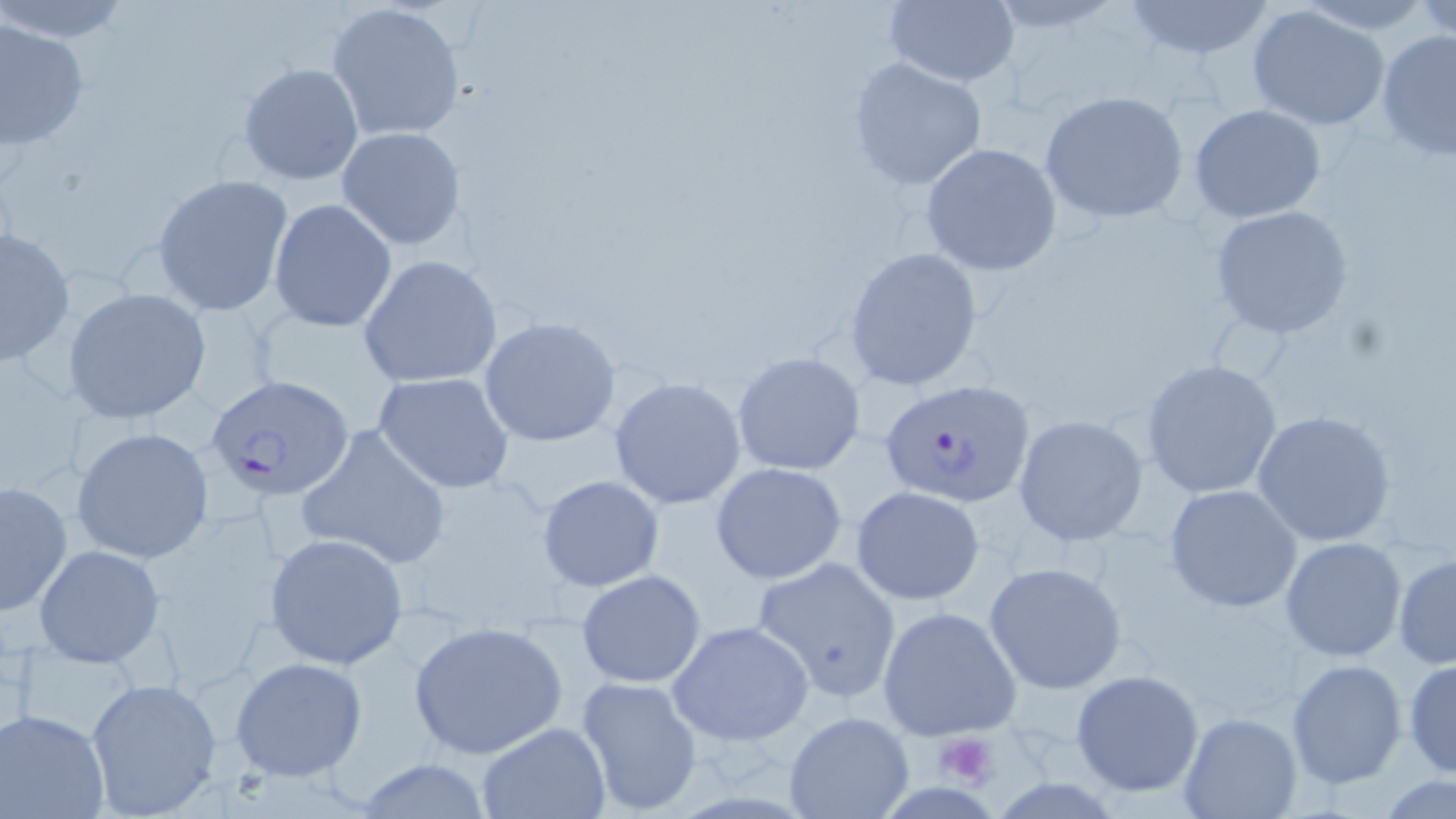

slide-level diagnosis = Plasmodium falciparum
field of view = one of a larger specimen
platelet locations = approximate bounding boxes as named x1/y1/x2/y2 corners in pixels: (x1=934, y1=731, x2=999, y2=787)
modality = light microscopy
image size = 1456×819 pixels
stain = May-Grünwald-Giemsa
uninfected red blood cell locations = approximate bounding boxes as named x1/y1/x2/y2 corners in pixels: (x1=1, y1=0, x2=133, y2=43), (x1=1416, y1=0, x2=1455, y2=40), (x1=325, y1=1, x2=469, y2=143), (x1=882, y1=1, x2=1021, y2=87), (x1=1118, y1=1, x2=1278, y2=60), (x1=1246, y1=5, x2=1392, y2=132), (x1=0, y1=17, x2=89, y2=151), (x1=1375, y1=29, x2=1456, y2=160), (x1=847, y1=58, x2=987, y2=192), (x1=238, y1=62, x2=364, y2=187), (x1=1039, y1=90, x2=1191, y2=225), (x1=1189, y1=103, x2=1328, y2=224), (x1=336, y1=125, x2=467, y2=249), (x1=920, y1=142, x2=1062, y2=277), (x1=150, y1=173, x2=295, y2=316), (x1=268, y1=198, x2=397, y2=334), (x1=1209, y1=205, x2=1356, y2=339), (x1=0, y1=226, x2=76, y2=368), (x1=844, y1=246, x2=986, y2=391), (x1=358, y1=254, x2=503, y2=389), (x1=63, y1=287, x2=212, y2=426), (x1=478, y1=316, x2=625, y2=449), (x1=733, y1=351, x2=867, y2=477), (x1=1140, y1=358, x2=1283, y2=499), (x1=372, y1=372, x2=516, y2=494), (x1=608, y1=377, x2=747, y2=509), (x1=1251, y1=409, x2=1398, y2=548), (x1=1012, y1=414, x2=1150, y2=546), (x1=297, y1=422, x2=451, y2=569), (x1=71, y1=426, x2=216, y2=565), (x1=710, y1=462, x2=849, y2=585), (x1=538, y1=474, x2=665, y2=592), (x1=0, y1=480, x2=73, y2=616), (x1=1164, y1=484, x2=1304, y2=614), (x1=850, y1=486, x2=987, y2=605), (x1=264, y1=533, x2=409, y2=670), (x1=1279, y1=536, x2=1407, y2=663), (x1=34, y1=544, x2=163, y2=667), (x1=1392, y1=553, x2=1456, y2=670), (x1=750, y1=555, x2=905, y2=705), (x1=984, y1=560, x2=1128, y2=694), (x1=576, y1=569, x2=706, y2=688), (x1=877, y1=605, x2=1023, y2=741), (x1=410, y1=619, x2=569, y2=761), (x1=667, y1=620, x2=814, y2=746), (x1=229, y1=656, x2=369, y2=783), (x1=1285, y1=658, x2=1407, y2=790), (x1=1403, y1=658, x2=1455, y2=779), (x1=1070, y1=669, x2=1205, y2=796), (x1=575, y1=675, x2=704, y2=813), (x1=84, y1=677, x2=224, y2=815), (x1=0, y1=709, x2=113, y2=819), (x1=784, y1=712, x2=913, y2=819), (x1=1177, y1=712, x2=1303, y2=818), (x1=474, y1=722, x2=612, y2=819), (x1=351, y1=759, x2=496, y2=817), (x1=1375, y1=775, x2=1456, y2=819)
preparation = thin blood film
Plasmodium falciparum-infected red blood cell locations = approximate bounding boxes as named x1/y1/x2/y2 corners in pixels: (x1=206, y1=374, x2=355, y2=502), (x1=877, y1=377, x2=1036, y2=507)
magnification = 1000x